Point out leukocytes.
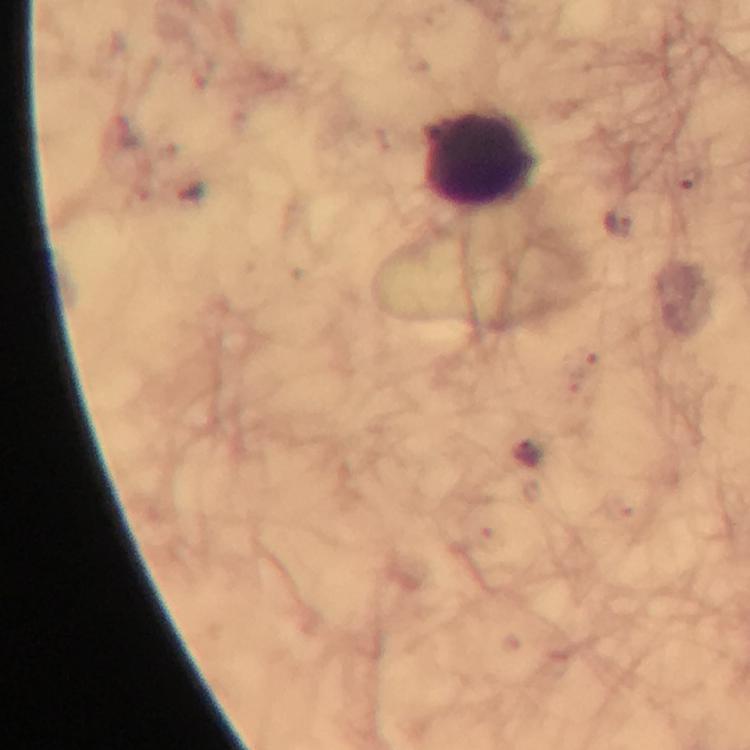
Approximate object centers, in pixels from the top-left corner.
Leukocytes: (x=478, y=160).

Malaria parasite locations: (x=619, y=225). Giemsa-stained preparation. Smartphone photograph taken through a microscope. Thick blood smear. Image is 750×750 pixels. From a diagnostic examination for malaria. At 100x magnification. Immersion oil applied. Cropped region of a single field of view.